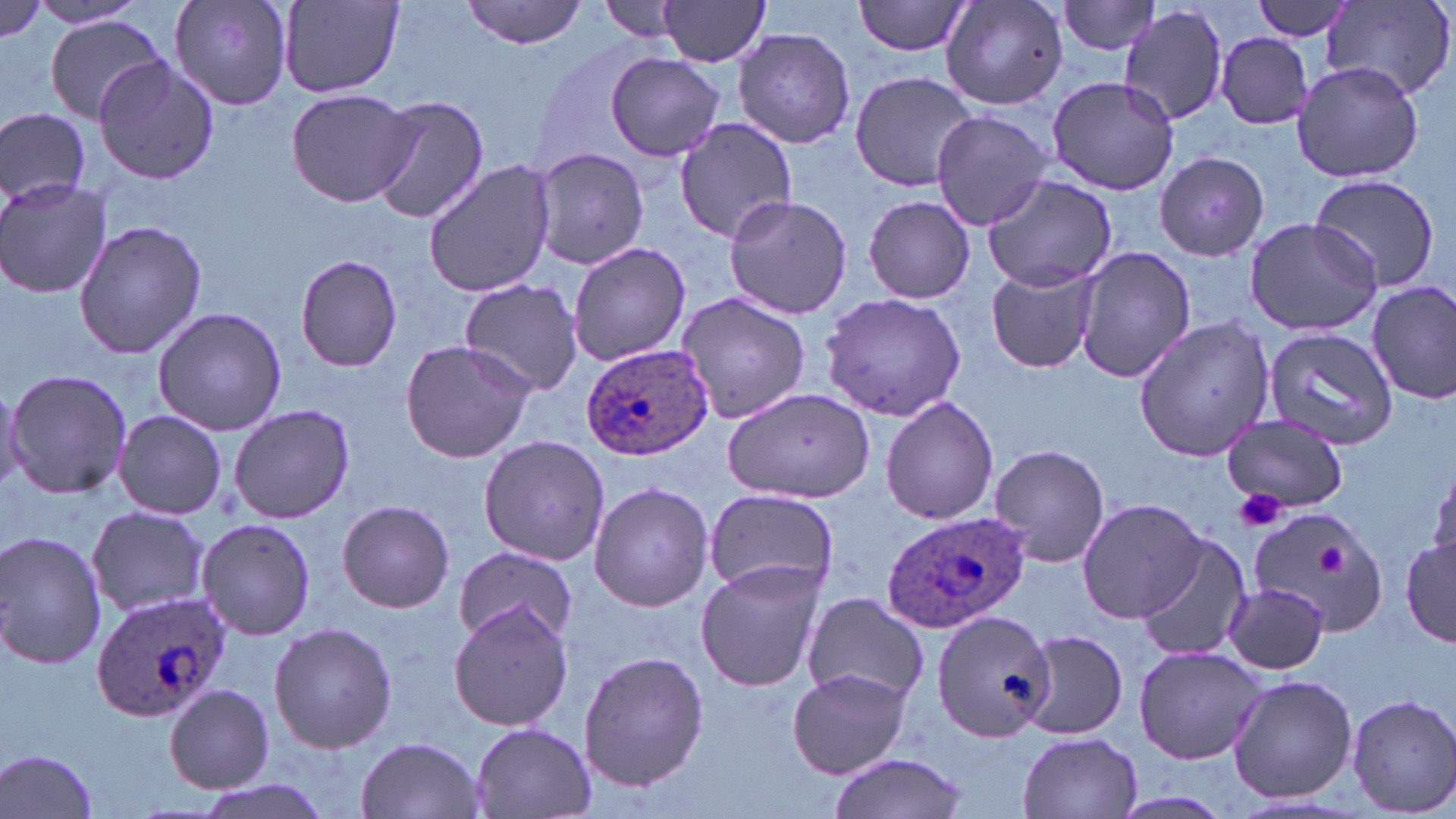

Approximate bounding boxes as [x1, y1, x2, y2] in pixels. Platelet locations: [1231, 488, 1287, 533], [1318, 544, 1346, 574]. Uninfected red blood cell locations: [0, 0, 53, 46], [29, 0, 150, 30], [170, 0, 293, 109], [599, 0, 691, 42], [854, 0, 977, 57], [940, 0, 1069, 108], [1248, 0, 1357, 40], [463, 1, 588, 48], [654, 1, 772, 67], [1055, 1, 1164, 56], [1323, 1, 1456, 102], [278, 2, 405, 96], [1117, 6, 1230, 127], [44, 17, 166, 125], [733, 27, 855, 150], [1213, 33, 1315, 129], [605, 53, 726, 161], [93, 57, 219, 185], [1291, 60, 1426, 185], [849, 71, 981, 191], [1046, 75, 1180, 197], [285, 86, 416, 207], [367, 96, 489, 224], [0, 107, 92, 207], [930, 109, 1054, 229], [673, 117, 800, 244], [529, 146, 651, 270], [1156, 151, 1271, 263], [424, 159, 556, 299], [1309, 172, 1442, 293], [981, 173, 1117, 293], [0, 177, 113, 300], [721, 193, 853, 318], [864, 194, 976, 304], [1243, 216, 1383, 337], [72, 219, 209, 361], [567, 241, 691, 368], [1072, 243, 1197, 383], [295, 253, 402, 373], [985, 263, 1102, 374], [458, 278, 587, 395], [1366, 281, 1456, 404], [676, 291, 811, 425], [820, 293, 968, 422], [152, 307, 288, 434], [1132, 314, 1276, 462], [1259, 326, 1400, 449], [398, 339, 537, 464], [4, 368, 133, 500], [0, 380, 26, 494], [720, 387, 876, 504], [880, 393, 999, 525], [227, 404, 356, 524], [113, 410, 227, 519], [1220, 414, 1350, 515], [478, 434, 610, 566], [988, 442, 1111, 569], [1426, 459, 1456, 578], [588, 481, 714, 612], [702, 486, 838, 601], [1078, 497, 1208, 622], [337, 499, 456, 613], [1252, 505, 1391, 635], [84, 506, 212, 619], [197, 517, 317, 641], [0, 531, 105, 669], [1134, 535, 1252, 663], [1402, 539, 1455, 648], [451, 547, 579, 643], [696, 561, 824, 692], [1225, 583, 1329, 674], [802, 590, 928, 707], [450, 602, 574, 731], [934, 610, 1056, 740], [268, 622, 398, 754], [1016, 630, 1130, 741], [1134, 645, 1263, 763], [577, 650, 712, 794], [787, 667, 912, 778], [1228, 674, 1357, 803], [164, 685, 275, 793], [1347, 694, 1456, 816], [468, 722, 596, 819], [1016, 732, 1143, 819], [355, 736, 486, 819], [0, 748, 103, 817], [823, 754, 969, 819], [190, 776, 336, 819], [1113, 791, 1232, 817]. Plasmodium ovale-infected red blood cell locations: [581, 341, 712, 461], [881, 511, 1031, 633], [89, 590, 230, 723]. Slide-level diagnosis: Plasmodium ovale. 1000x magnification. Optical microscopy. Single field of view. Image is 1456×819 pixels. May-Grünwald-Giemsa stain. Thin blood smear.